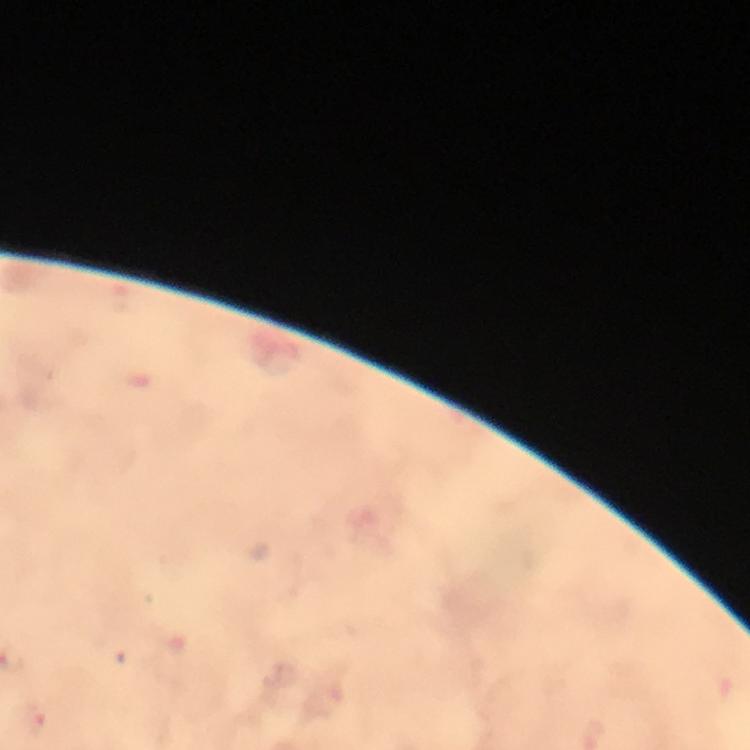

Approximate centers as (x, y) in pixels.
Summary:
  - Malaria parasite locations: (34, 722)
  - Stain: Giemsa
  - Immersion oil: applied
  - Magnification: 100x
  - Capture: smartphone camera through the microscope
  - Cropped from: one field of view
  - Context: from a malaria diagnostic workup
  - Preparation: thick blood smear
  - Image size: 750×750 pixels